Report the malaria status of this cell.
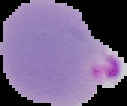

Parasitized.

Summary:
  - Image size: 127×106 pixels
  - Preparation: thin blood smear
  - Image type: segmented cell region on a black background